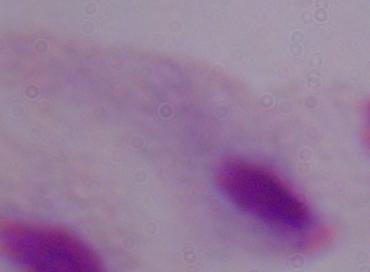
Summary:
  - Magnification: 1000x
  - Modality: micrograph
  - Identification: trichomonad